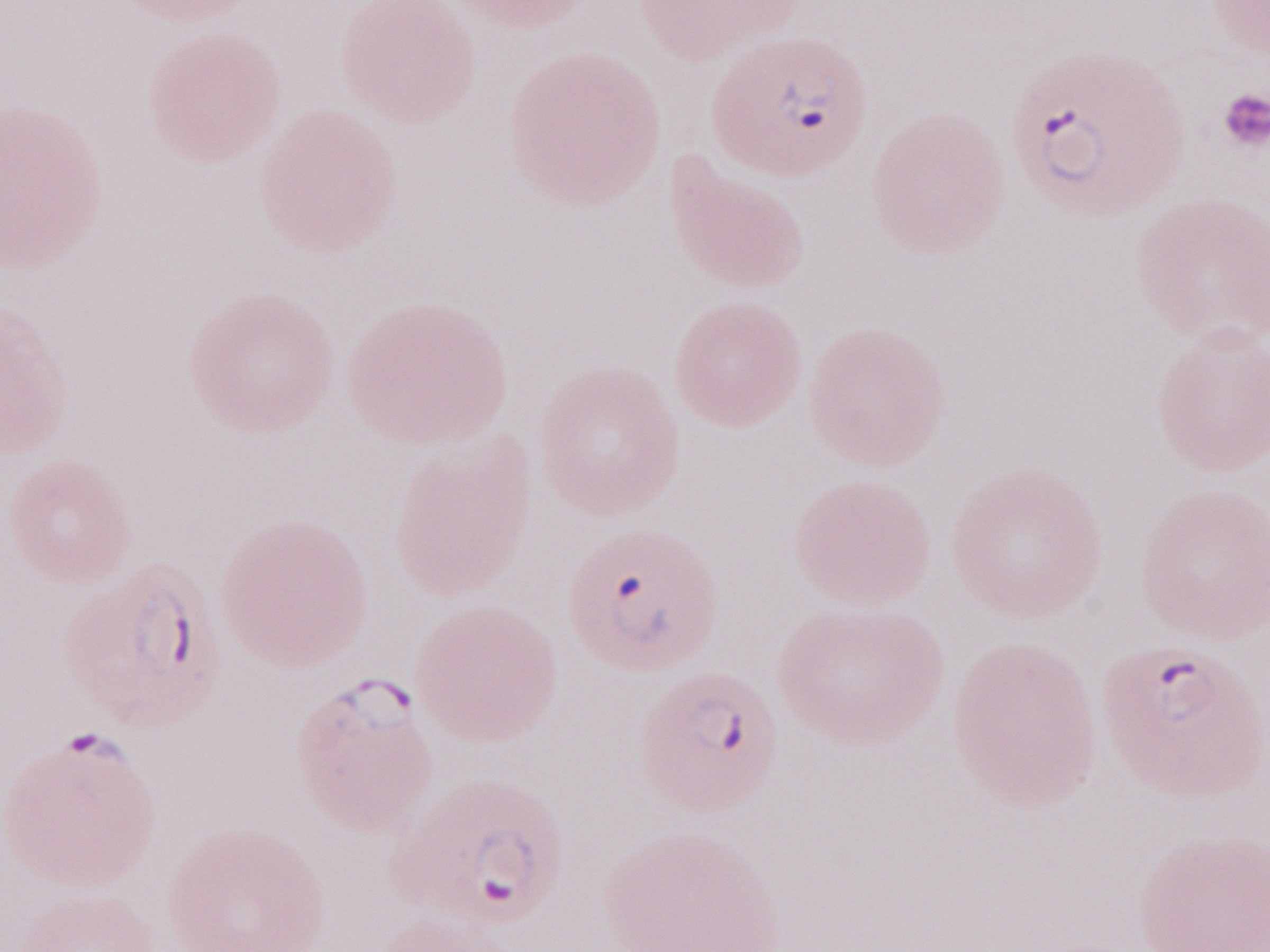 May-Grünwald-Giemsa stain. Image is 1270×952 pixels. Single field of view. Olympus BX43 microscope and DP73 digital camera. Thin peripheral-blood smear. Patient-level malaria diagnosis: positive. Magnification: 1,000x.